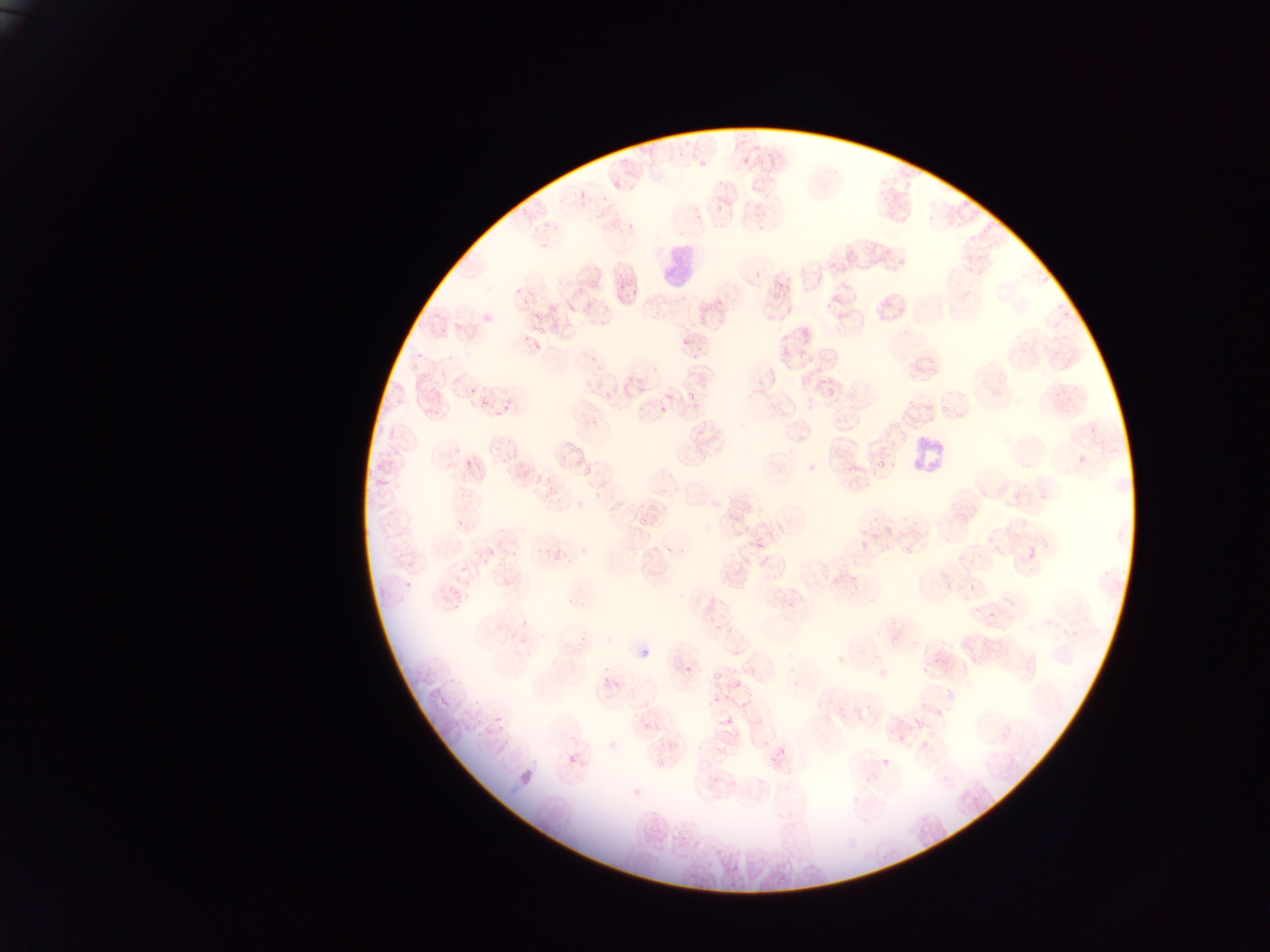
country: Ghana
field_of_view: single
leukocyte_locations: 'approximate bounding boxes as {left, top, right, bottom} in pixels: {653, 239, 699, 291}, {902, 423, 938, 473}, {884, 524, 890, 534}'
plasmodium_parasite_locations: 'approximate bounding boxes as {left, top, right, bottom} in pixels: {698, 153, 710, 172}, {742, 153, 753, 165}, {611, 176, 620, 189}, {581, 192, 593, 211}, {600, 193, 608, 204}, {713, 202, 724, 211}, {690, 203, 702, 213}, {541, 217, 555, 229}, {623, 219, 635, 233}, {895, 256, 906, 267}, {887, 268, 898, 275}, {626, 270, 635, 288}, {613, 273, 623, 286}, {616, 295, 626, 304}, {512, 297, 529, 310}, {715, 298, 724, 304}, {528, 305, 546, 318}, {584, 305, 593, 319}, {783, 305, 794, 312}, {767, 313, 781, 323}, {536, 323, 548, 337}, {436, 326, 446, 338}, {800, 330, 808, 339}, {682, 335, 693, 345}, {774, 339, 794, 356}, {777, 354, 788, 365}, {410, 361, 419, 371}, {913, 364, 922, 370}, {929, 365, 938, 375}, {766, 368, 777, 379}, {800, 368, 815, 379}, {622, 371, 631, 391}, {752, 380, 764, 389}, {468, 381, 477, 393}, {828, 389, 837, 396}, {504, 394, 512, 412}, {687, 398, 704, 415}, {940, 402, 953, 414}, {658, 405, 668, 414}, {490, 409, 497, 420}, {952, 409, 962, 420}, {589, 416, 599, 427}, {833, 416, 844, 427}, {888, 419, 898, 431}, {796, 436, 805, 445}, {494, 438, 502, 453}, {558, 438, 573, 451}, {448, 444, 464, 454}, {570, 447, 593, 456}, {696, 447, 708, 461}, {560, 452, 568, 468}, {463, 453, 478, 468}, {889, 458, 895, 468}, {511, 460, 521, 477}, {876, 460, 883, 469}, {844, 465, 855, 474}, {582, 466, 594, 479}, {528, 475, 542, 493}, {547, 480, 555, 492}, {846, 480, 855, 488}, {459, 488, 468, 499}, {1005, 488, 1022, 499}, {955, 505, 970, 522}, {638, 516, 649, 530}, {758, 520, 764, 530}, {985, 529, 1002, 541}, {738, 531, 750, 542}, {753, 531, 760, 542}, {860, 539, 870, 549}, {755, 542, 764, 552}, {498, 545, 511, 556}, {543, 546, 553, 557}, {904, 546, 915, 556}, {511, 550, 520, 559}, {751, 558, 765, 569}, {496, 573, 505, 584}, {784, 591, 795, 610}, {449, 598, 463, 613}, {1005, 598, 1016, 607}, {520, 618, 528, 628}, {724, 625, 734, 634}, {723, 665, 737, 676}, {684, 666, 690, 675}, {919, 668, 928, 675}, {711, 671, 722, 682}, {599, 673, 613, 692}, {731, 679, 740, 688}, {611, 680, 622, 692}, {723, 693, 731, 703}, {712, 694, 721, 703}, {438, 697, 447, 707}, {739, 701, 748, 712}, {933, 708, 943, 717}, {724, 717, 733, 726}, {915, 717, 925, 727}, {639, 720, 653, 731}, {483, 725, 494, 736}, {1001, 731, 1010, 741}, {919, 735, 927, 749}, {762, 739, 770, 747}, {607, 740, 617, 750}, {777, 740, 790, 754}, {655, 752, 666, 768}, {568, 754, 578, 764}, {882, 758, 889, 767}, {972, 797, 981, 807}, {723, 861, 738, 874}, {775, 876, 791, 889}, {696, 877, 709, 883}, {724, 881, 742, 895} | approximate {x, y} pixel centers of objects too small to bound: {692, 396}, {746, 509}, {458, 524}'
image_size: 1270×952 pixels
capture: mobile-phone photograph through a microscope
preparation: thin blood film